Locate and identify every blood parasite.
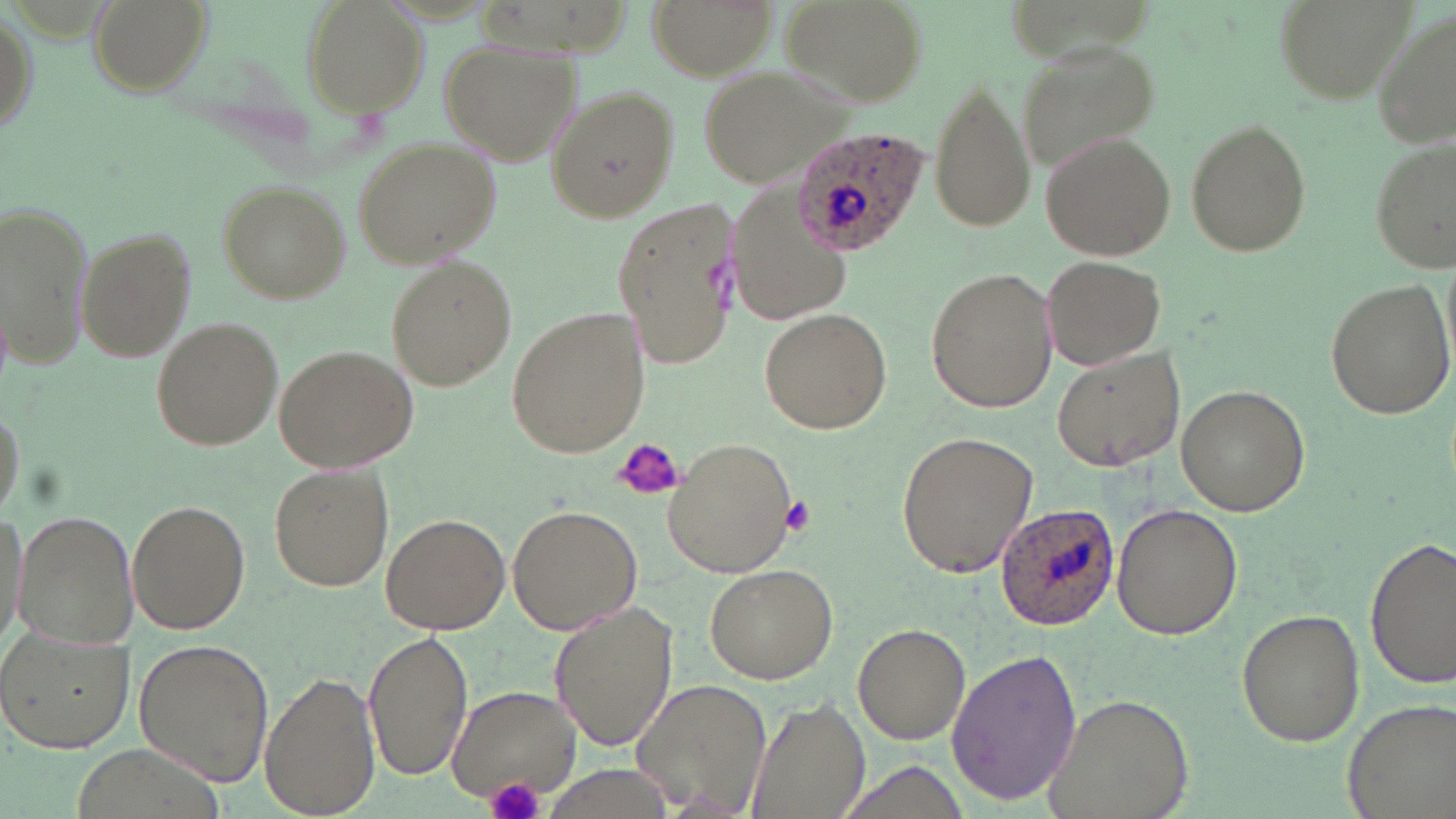
Approximate bounding boxes as [x1, y1, x2, y2] in pixels.
Plasmodium ovale-infected red blood cells: [790, 125, 928, 257], [996, 504, 1118, 630].
No Plasmodium falciparum, Plasmodium malariae, Plasmodium vivax, Babesia divergens, or Trypanosoma brucei observed.

Summary:
  - Platelet locations: [611, 439, 683, 503], [780, 497, 816, 534], [485, 776, 545, 819]
  - Uninfected red blood cell locations: [90, 0, 213, 101], [301, 0, 429, 117], [643, 0, 779, 81], [782, 0, 928, 108], [1274, 0, 1421, 107], [0, 3, 40, 148], [1369, 10, 1456, 150], [439, 39, 579, 167], [1015, 39, 1158, 175], [700, 64, 854, 190], [929, 80, 1035, 233], [543, 85, 680, 225], [1183, 120, 1314, 259], [1040, 131, 1176, 259], [1369, 133, 1455, 272], [351, 136, 502, 271], [216, 180, 348, 301], [730, 180, 856, 327], [610, 198, 743, 373], [2, 201, 95, 369], [74, 226, 197, 363], [1042, 253, 1166, 369], [382, 256, 517, 392], [924, 265, 1060, 413], [1323, 275, 1454, 420], [503, 302, 653, 460], [760, 307, 892, 433], [152, 316, 283, 450], [1052, 343, 1188, 472], [274, 344, 417, 472], [1175, 384, 1312, 515], [895, 430, 1038, 581], [664, 437, 798, 581], [270, 463, 395, 591], [126, 497, 251, 632], [1110, 503, 1243, 640], [507, 504, 641, 633], [13, 509, 139, 648], [381, 512, 511, 635], [1366, 539, 1455, 689], [703, 563, 839, 683], [548, 600, 678, 755], [1238, 607, 1365, 748], [853, 623, 971, 745], [365, 628, 469, 782], [0, 630, 136, 752], [132, 638, 274, 784], [944, 648, 1083, 805], [261, 671, 380, 817], [632, 679, 772, 816], [447, 684, 580, 804], [1040, 693, 1193, 819], [744, 695, 868, 819], [1340, 696, 1456, 819], [833, 760, 975, 819]
  - Slide-level diagnosis: Plasmodium ovale
  - Field of view: one of a larger specimen
  - Preparation: thin blood film
  - Image size: 1456×819 pixels
  - Modality: light microscopy
  - Magnification: 1000x
  - Stain: May-Grünwald-Giemsa